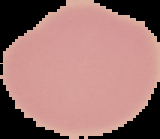

malaria status = uninfected
image size = 160×139 pixels
image type = cell region segmented out of the field of view; surrounding area masked to black
preparation = thin blood film